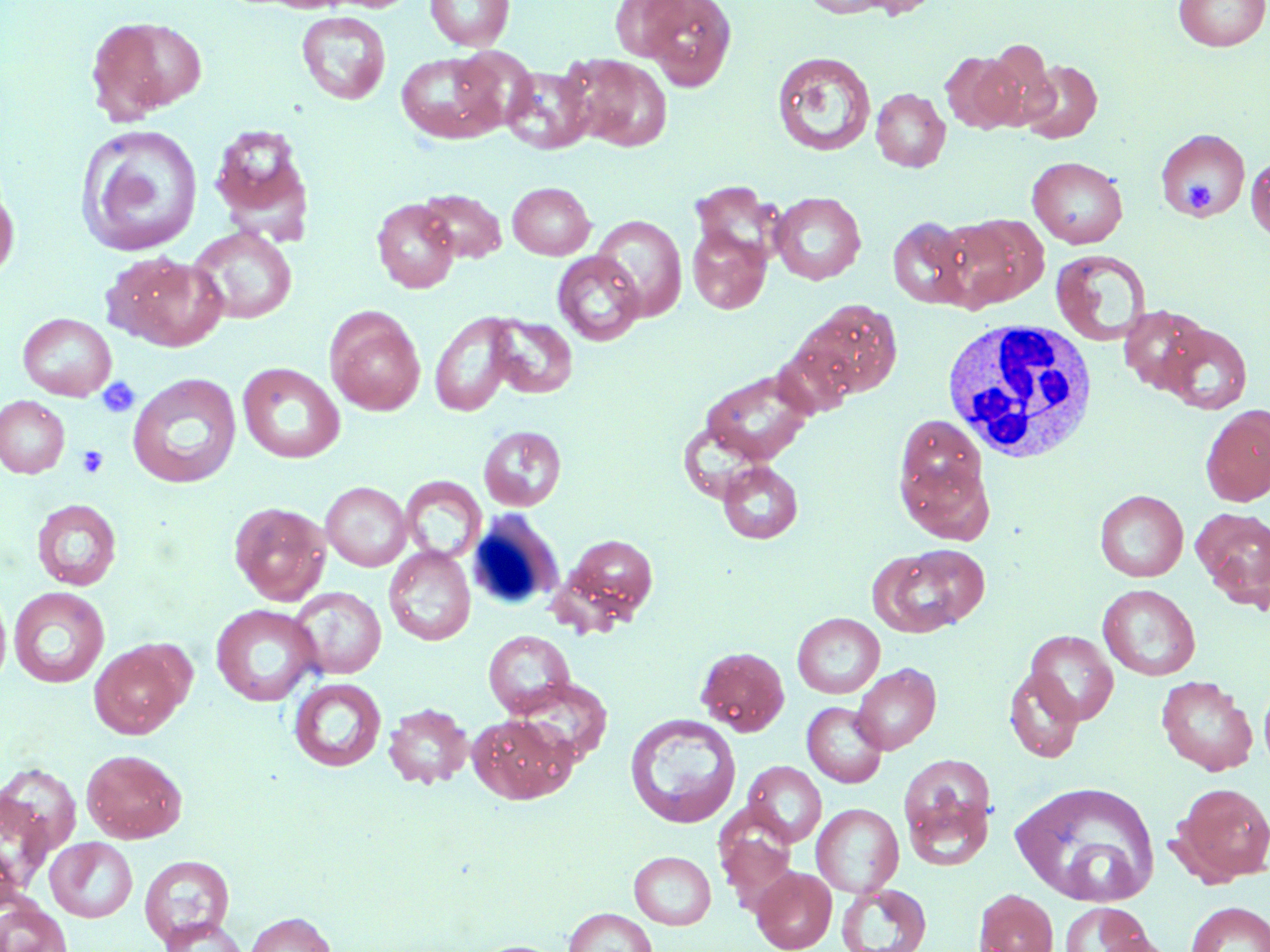
{
  "slide_level_diagnosis": "no evidence of blood parasites",
  "platelet_locations": "approximate bounding boxes as (x1,y1)-(x2,y2) corner pairs in pixels: (1182,180)-(1217,217), (96,377)-(141,418), (76,445)-(109,478)",
  "field_of_view": "single",
  "magnification": "1000x",
  "stain": "May-Grünwald-Giemsa",
  "white_blood_cell_locations": "approximate bounding boxes as (x1,y1)-(x2,y2) corner pairs in pixels: (942,317)-(1099,464), (466,510)-(565,613)",
  "uninfected_red_blood_cell_locations": "approximate bounding boxes as (x1,y1)-(x2,y2) corner pairs in pixels: (424,0)-(515,51), (608,0)-(691,60), (641,0)-(736,90), (802,0)-(898,18), (848,0)-(943,19), (1174,0)-(1269,51), (297,11)-(391,105), (85,16)-(207,122), (980,40)-(1057,129), (451,46)-(537,133), (395,51)-(506,144), (771,51)-(876,157), (940,51)-(1026,133), (566,54)-(672,151), (1019,59)-(1102,144), (501,67)-(596,154), (870,88)-(951,172), (209,123)-(313,235), (76,124)-(204,256), (1156,129)-(1250,220), (1246,155)-(1270,241), (1027,156)-(1128,248), (0,177)-(19,284), (690,181)-(785,268), (507,182)-(595,260), (418,189)-(507,264), (770,192)-(866,284), (372,199)-(460,293), (942,214)-(1048,311), (591,215)-(687,321), (887,217)-(974,308), (189,226)-(297,324), (687,226)-(771,314), (1051,250)-(1151,347), (552,251)-(645,346), (103,253)-(228,351), (790,300)-(903,402), (1118,304)-(1211,394), (325,307)-(425,416), (430,312)-(519,417), (18,313)-(117,401), (487,316)-(577,398), (1160,324)-(1253,414), (770,341)-(858,420), (237,363)-(346,464), (700,369)-(816,467), (128,373)-(242,489), (0,396)-(70,478), (1200,404)-(1270,507), (896,415)-(986,508), (479,426)-(566,511), (900,458)-(996,545), (717,461)-(803,544), (399,476)-(486,563), (321,482)-(412,571), (1095,489)-(1188,582), (31,499)-(122,591), (228,501)-(331,606), (1194,508)-(1270,608), (558,533)-(660,626), (873,545)-(988,636), (384,546)-(476,646), (0,583)-(12,692), (1098,584)-(1200,681), (9,586)-(110,688), (288,587)-(387,679), (211,604)-(321,706), (792,612)-(885,699), (483,630)-(575,717), (1025,630)-(1118,724), (89,640)-(191,738), (696,646)-(790,736), (852,663)-(941,755), (1003,667)-(1085,763), (1156,675)-(1258,776), (289,677)-(386,772), (509,677)-(613,767), (1258,680)-(1270,776), (802,702)-(887,787), (384,703)-(473,790), (469,713)-(576,803), (625,714)-(741,829), (81,749)-(187,843), (897,754)-(997,865), (743,761)-(826,847), (0,762)-(82,858), (1009,780)-(1160,907), (1173,783)-(1270,885), (0,789)-(55,899), (812,803)-(904,897), (715,807)-(800,909), (46,837)-(138,922), (629,851)-(716,929), (139,854)-(235,948), (751,866)-(837,952), (837,883)-(932,952), (974,887)-(1058,952), (0,899)-(72,952), (1185,901)-(1270,952), (1060,902)-(1153,952), (563,907)-(657,952), (244,912)-(335,952), (159,916)-(250,951), (1091,934)-(1182,952), (466,940)-(568,952)",
  "preparation": "thin blood smear",
  "modality": "optical microscopy",
  "image_size": "1270×952 pixels"
}